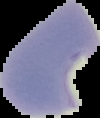
image size = 100×118 pixels
result = malaria parasites identified
image type = cell region segmented out of the field of view; surrounding area masked to black
preparation = thin blood smear